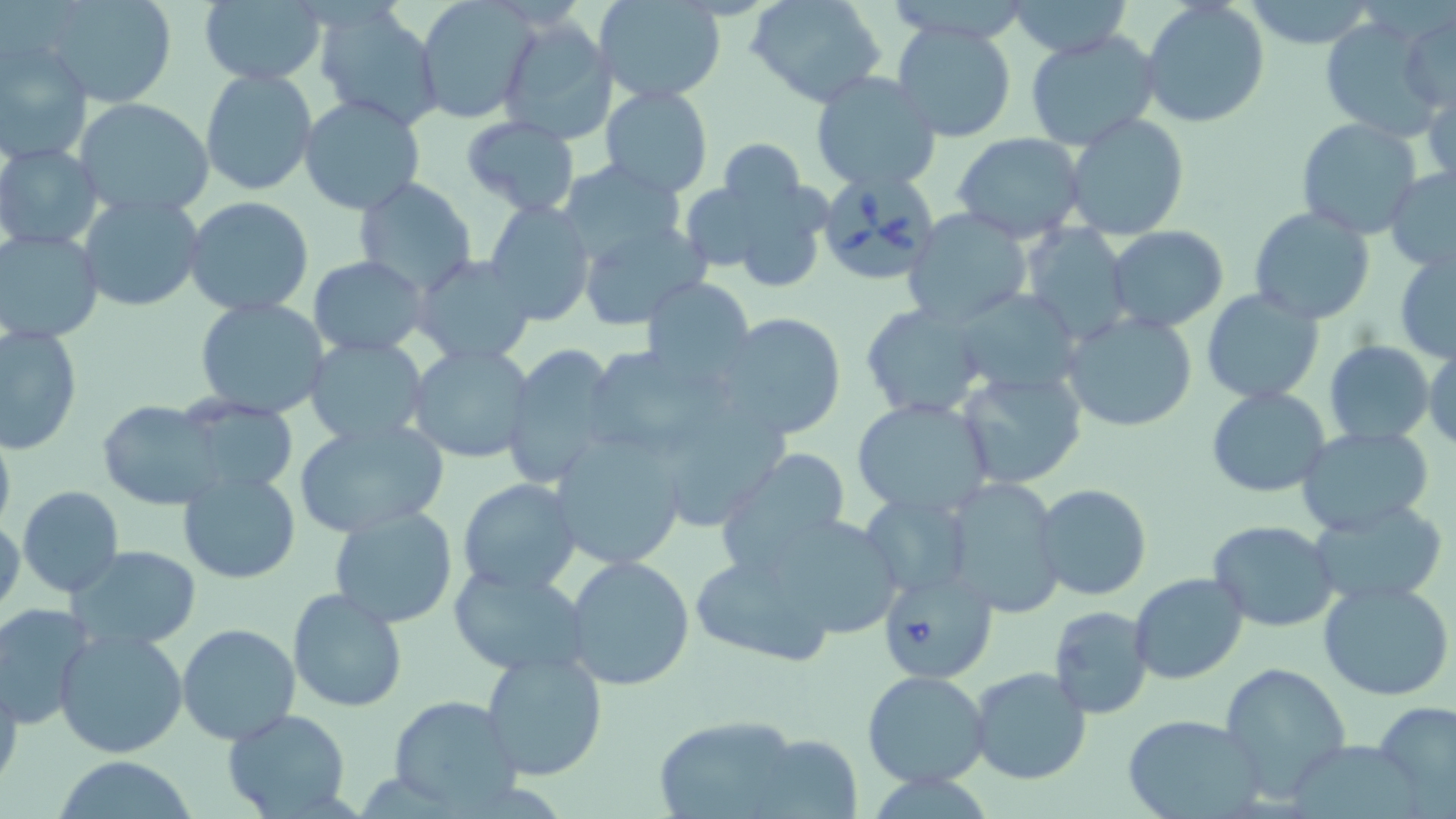

Summary:
  - Coordinate format: approximate bounding boxes as named x1/y1/x2/y2 corners in pixels
  - Babesia divergens-infected red blood cell locations: (x1=811, y1=165, x2=936, y2=280), (x1=876, y1=567, x2=997, y2=684)
  - Uninfected red blood cell locations: (x1=39, y1=0, x2=180, y2=109), (x1=414, y1=0, x2=538, y2=125), (x1=1007, y1=0, x2=1132, y2=58), (x1=198, y1=1, x2=327, y2=85), (x1=596, y1=1, x2=727, y2=103), (x1=749, y1=1, x2=886, y2=108), (x1=1141, y1=1, x2=1271, y2=128), (x1=1243, y1=1, x2=1379, y2=49), (x1=314, y1=5, x2=442, y2=131), (x1=1399, y1=9, x2=1455, y2=114), (x1=1322, y1=13, x2=1442, y2=143), (x1=497, y1=16, x2=618, y2=145), (x1=890, y1=20, x2=1018, y2=143), (x1=1023, y1=29, x2=1164, y2=153), (x1=0, y1=38, x2=95, y2=163), (x1=199, y1=68, x2=319, y2=196), (x1=810, y1=72, x2=942, y2=193), (x1=1424, y1=75, x2=1455, y2=195), (x1=600, y1=87, x2=713, y2=196), (x1=299, y1=94, x2=426, y2=215), (x1=73, y1=97, x2=218, y2=222), (x1=1063, y1=112, x2=1190, y2=242), (x1=460, y1=116, x2=580, y2=217), (x1=1296, y1=118, x2=1423, y2=239), (x1=952, y1=131, x2=1088, y2=243), (x1=718, y1=139, x2=807, y2=215), (x1=0, y1=143, x2=103, y2=250), (x1=556, y1=158, x2=689, y2=268), (x1=1384, y1=165, x2=1456, y2=273), (x1=687, y1=173, x2=830, y2=292), (x1=352, y1=178, x2=478, y2=297), (x1=77, y1=194, x2=205, y2=313), (x1=183, y1=198, x2=314, y2=316), (x1=484, y1=200, x2=596, y2=327), (x1=1249, y1=205, x2=1377, y2=325), (x1=904, y1=209, x2=1033, y2=329), (x1=577, y1=221, x2=707, y2=326), (x1=1023, y1=225, x2=1134, y2=346), (x1=1105, y1=225, x2=1230, y2=332), (x1=1, y1=229, x2=104, y2=344), (x1=1394, y1=249, x2=1456, y2=365), (x1=308, y1=255, x2=428, y2=356), (x1=413, y1=255, x2=537, y2=367), (x1=642, y1=275, x2=756, y2=386), (x1=952, y1=288, x2=1086, y2=396), (x1=1202, y1=288, x2=1324, y2=404), (x1=193, y1=297, x2=332, y2=421), (x1=1079, y1=298, x2=1328, y2=414), (x1=862, y1=304, x2=989, y2=419), (x1=1061, y1=310, x2=1197, y2=434), (x1=716, y1=312, x2=848, y2=441), (x1=0, y1=323, x2=82, y2=455), (x1=304, y1=336, x2=429, y2=448), (x1=1323, y1=341, x2=1435, y2=445), (x1=408, y1=344, x2=537, y2=464), (x1=1424, y1=344, x2=1455, y2=452), (x1=503, y1=345, x2=619, y2=492), (x1=589, y1=345, x2=739, y2=450), (x1=954, y1=367, x2=1088, y2=489), (x1=1206, y1=387, x2=1331, y2=496), (x1=851, y1=396, x2=995, y2=520), (x1=177, y1=399, x2=301, y2=498), (x1=100, y1=401, x2=228, y2=510), (x1=673, y1=413, x2=795, y2=528), (x1=294, y1=416, x2=448, y2=539), (x1=0, y1=424, x2=16, y2=539), (x1=1295, y1=425, x2=1435, y2=536), (x1=547, y1=431, x2=687, y2=571), (x1=716, y1=447, x2=855, y2=577), (x1=177, y1=471, x2=304, y2=585), (x1=457, y1=477, x2=582, y2=594), (x1=946, y1=477, x2=1067, y2=619), (x1=1036, y1=484, x2=1151, y2=601), (x1=16, y1=487, x2=124, y2=597), (x1=862, y1=491, x2=972, y2=598), (x1=1306, y1=498, x2=1449, y2=604), (x1=328, y1=504, x2=459, y2=628), (x1=756, y1=512, x2=907, y2=641), (x1=1, y1=514, x2=24, y2=622), (x1=303, y1=517, x2=439, y2=695), (x1=1208, y1=521, x2=1340, y2=632), (x1=69, y1=545, x2=201, y2=650), (x1=689, y1=548, x2=843, y2=670), (x1=564, y1=554, x2=696, y2=691), (x1=446, y1=564, x2=593, y2=676), (x1=1128, y1=573, x2=1249, y2=684), (x1=1317, y1=580, x2=1456, y2=703), (x1=287, y1=587, x2=410, y2=713), (x1=0, y1=603, x2=92, y2=731), (x1=1048, y1=606, x2=1154, y2=719), (x1=176, y1=622, x2=301, y2=745), (x1=53, y1=624, x2=189, y2=759), (x1=480, y1=649, x2=608, y2=781), (x1=1221, y1=663, x2=1350, y2=796), (x1=0, y1=664, x2=23, y2=794), (x1=968, y1=665, x2=1093, y2=785), (x1=863, y1=671, x2=991, y2=788), (x1=388, y1=696, x2=523, y2=813), (x1=1376, y1=701, x2=1456, y2=810), (x1=222, y1=709, x2=352, y2=818), (x1=1121, y1=713, x2=1266, y2=819), (x1=650, y1=714, x2=809, y2=819), (x1=745, y1=732, x2=863, y2=819), (x1=54, y1=757, x2=197, y2=818)
  - Slide-level diagnosis: Babesia divergens
  - Image size: 1456×819 pixels
  - Modality: optical microscopy
  - Stain: May-Grünwald-Giemsa
  - Field of view: one of a larger specimen
  - Magnification: 1000x
  - Preparation: thin blood smear